Name the parasite shown.
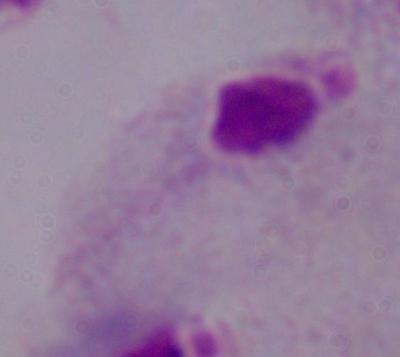
This is a trichomonad.

{
  "modality": "micrograph",
  "magnification": "1000x"
}